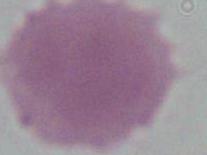

Summary:
  - Magnification: 1000x
  - Modality: micrograph
  - Identification: erythrocyte